Classify this cell by malaria status.
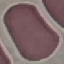
It is uninfected.

image type = automatically extracted cell patch, resized to 64 × 64 pixels
preparation = thin blood film
stain = Giemsa
capture = smartphone camera at the microscope eyepiece